Locate every blood parasite and identify its species.
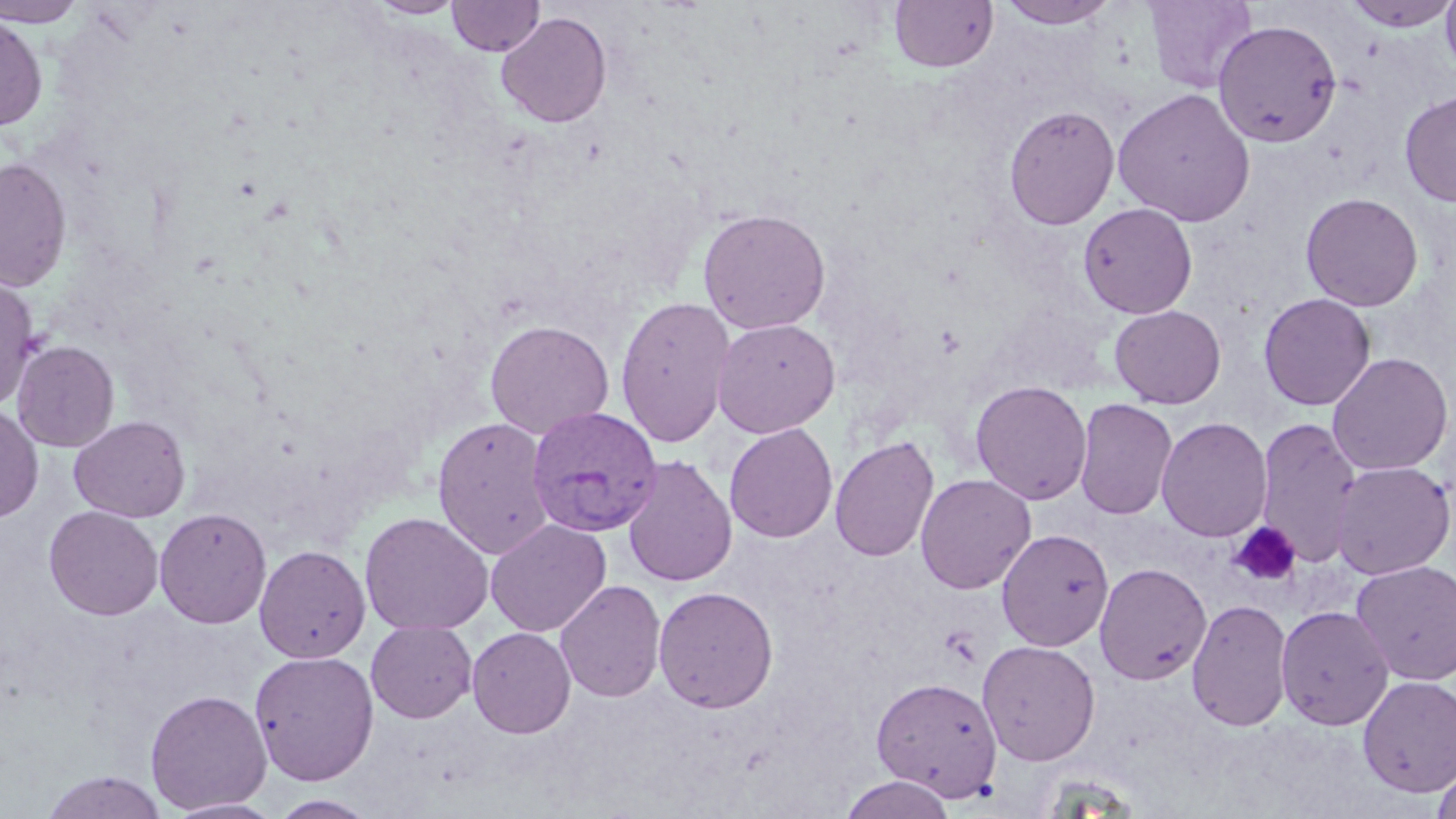

Approximate bounding boxes as [x1, y1, x2, y2] in pixels.
Plasmodium vivax-infected red blood cells: [526, 406, 664, 537].
No Plasmodium falciparum, Plasmodium ovale, Plasmodium malariae, Babesia divergens, or Trypanosoma brucei observed.

Summary:
  - Platelet locations: [1228, 521, 1302, 588], [939, 625, 982, 667]
  - Uninfected red blood cell locations: [0, 0, 86, 27], [367, 0, 466, 19], [889, 0, 998, 74], [995, 0, 1120, 29], [1143, 0, 1257, 93], [1343, 0, 1456, 32], [1440, 0, 1456, 79], [447, 1, 545, 57], [496, 12, 612, 128], [0, 14, 48, 131], [1213, 19, 1342, 147], [1112, 87, 1256, 227], [1399, 91, 1456, 207], [1004, 104, 1120, 230], [0, 157, 73, 292], [1300, 192, 1424, 311], [1078, 202, 1198, 319], [696, 207, 832, 335], [0, 273, 40, 409], [1258, 293, 1376, 411], [615, 296, 736, 448], [1110, 305, 1227, 409], [711, 317, 841, 438], [484, 319, 614, 439], [11, 340, 119, 452], [1326, 352, 1454, 476], [970, 380, 1092, 505], [1073, 397, 1178, 520], [0, 405, 43, 523], [68, 415, 191, 522], [432, 416, 555, 559], [1256, 416, 1362, 568], [1156, 417, 1273, 541], [724, 423, 838, 543], [830, 436, 939, 563], [621, 455, 738, 587], [1330, 461, 1455, 580], [915, 473, 1036, 594], [44, 506, 164, 620], [154, 507, 272, 628], [360, 511, 494, 635], [485, 518, 611, 636], [996, 529, 1113, 651], [254, 544, 371, 663], [1350, 559, 1456, 686], [1094, 562, 1212, 685], [555, 579, 666, 703], [652, 585, 779, 713], [1186, 597, 1294, 732], [1275, 604, 1394, 730], [365, 620, 477, 723], [467, 626, 576, 738], [977, 639, 1101, 765], [250, 650, 379, 786], [1357, 675, 1456, 798], [871, 676, 1003, 801], [144, 689, 272, 814], [1432, 760, 1456, 819], [40, 771, 167, 819], [839, 774, 956, 818], [267, 794, 382, 818], [166, 798, 285, 818]
  - Slide-level diagnosis: Plasmodium vivax
  - Magnification: 1000x
  - Field of view: single
  - Image size: 1456×819 pixels
  - Preparation: thin blood smear
  - Modality: light microscopy
  - Stain: May-Grünwald-Giemsa